Assess for malaria.
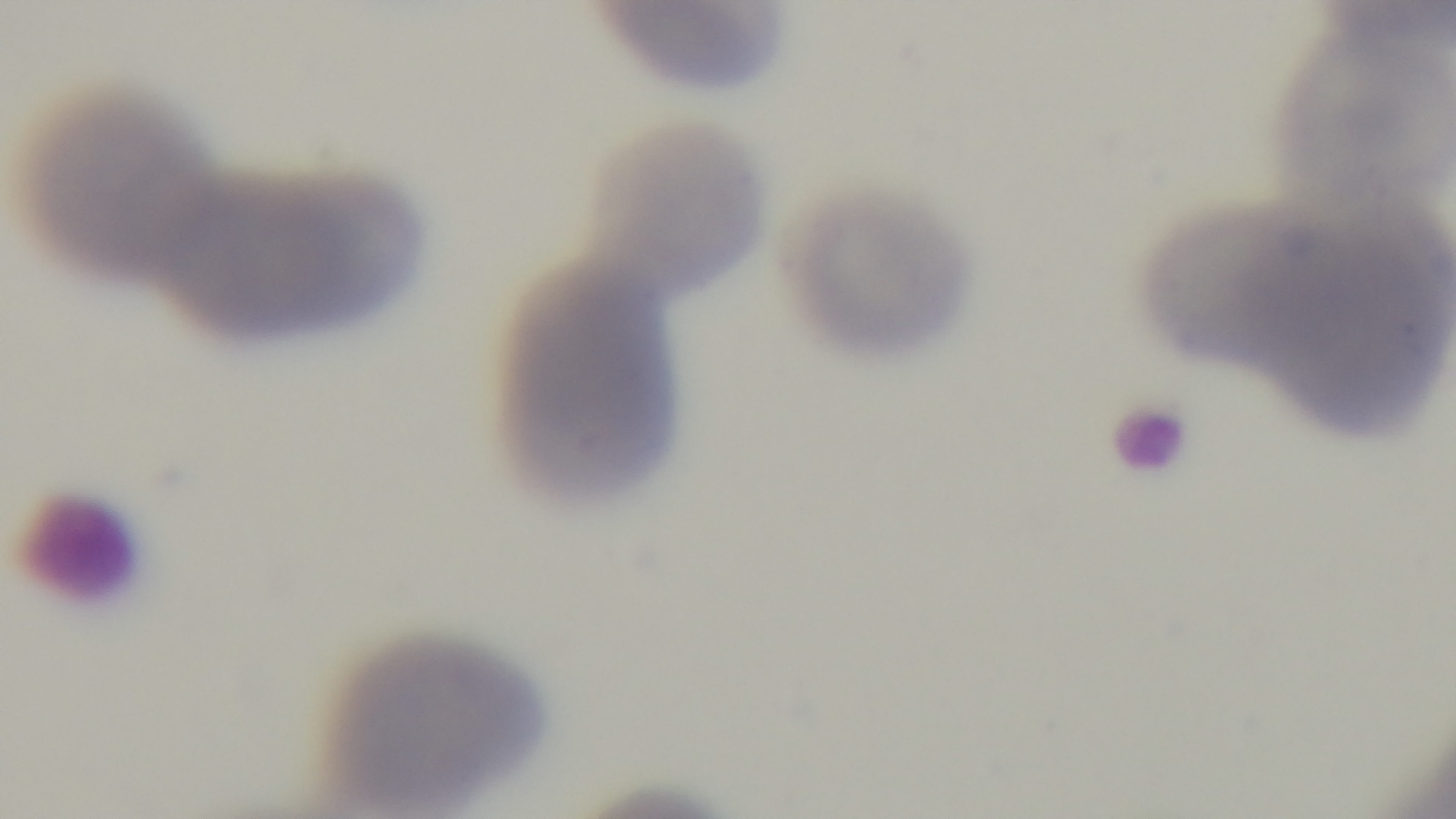
Negative.

{
  "preparation": "thin blood film",
  "field_of_view": "one from the slide",
  "stain": "Giemsa",
  "objective": "100x oil immersion",
  "capture": "mounted 4K digital camera",
  "modality": "light microscopy"
}